Look for Plasmodium parasites.
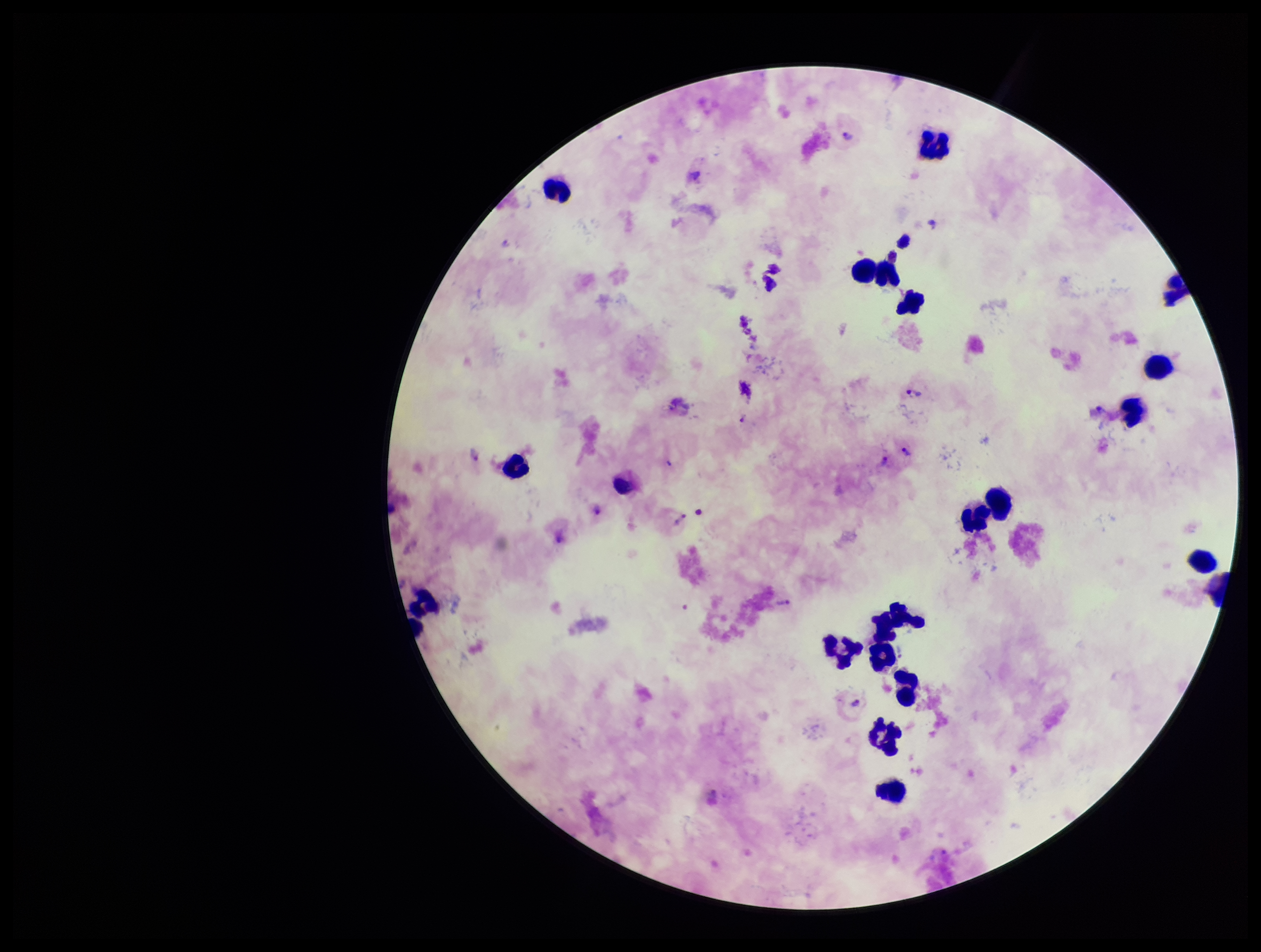

Detected.

Single field of view. Photographed through the microscope eyepiece with a smartphone camera. Patient malaria status: positive. Species reported for this patient: Plasmodium vivax. Giemsa stain. Parasite count: 11. Preparation: thick. Leukocyte count: 20. Image is 1261×952 pixels.